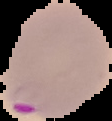
Summary:
  - Preparation: thin blood smear
  - Result: malaria parasites identified
  - Image size: 112×121 pixels
  - Image type: segmented cell region on a black background